Name the parasite shown.
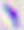

This is Toxoplasma gondii.

{
  "magnification": "400x",
  "modality": "micrograph"
}